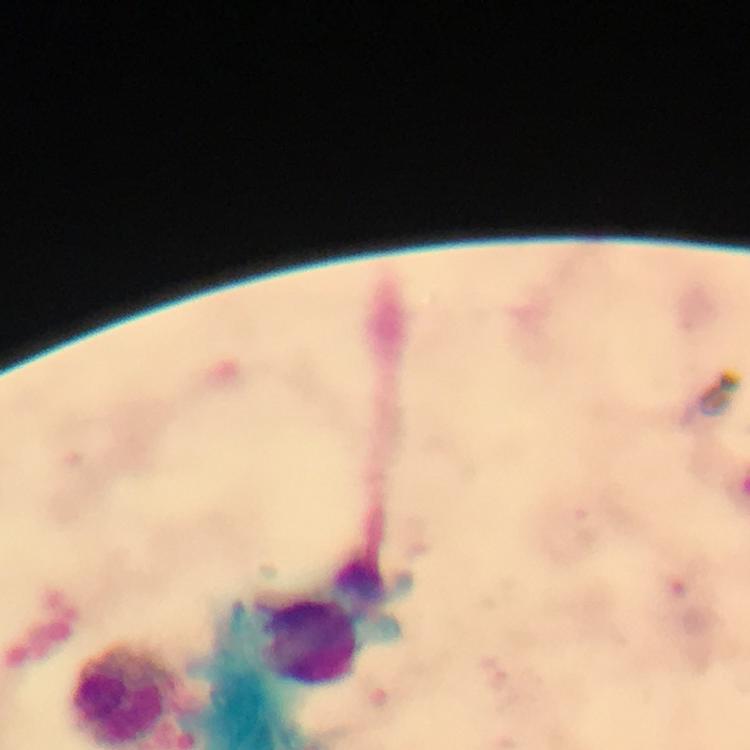
{
  "magnification": "100x",
  "immersion_oil": "applied",
  "capture": "smartphone camera through the microscope",
  "context": "from a diagnostic examination for malaria",
  "preparation": "thick blood film",
  "cropped_from": "one field of view",
  "stain": "Giemsa",
  "plasmodium_parasites": "none seen",
  "image_size": "750×750 pixels",
  "leukocyte_locations": "approximate centers as (x, y) in pixels: (312, 642), (120, 697)"
}